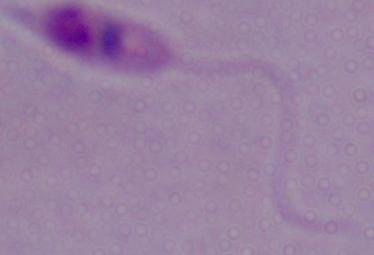
identification = Leishmania
magnification = 1000x
modality = photomicrograph